Give a bounding box for every leukocyte visible.
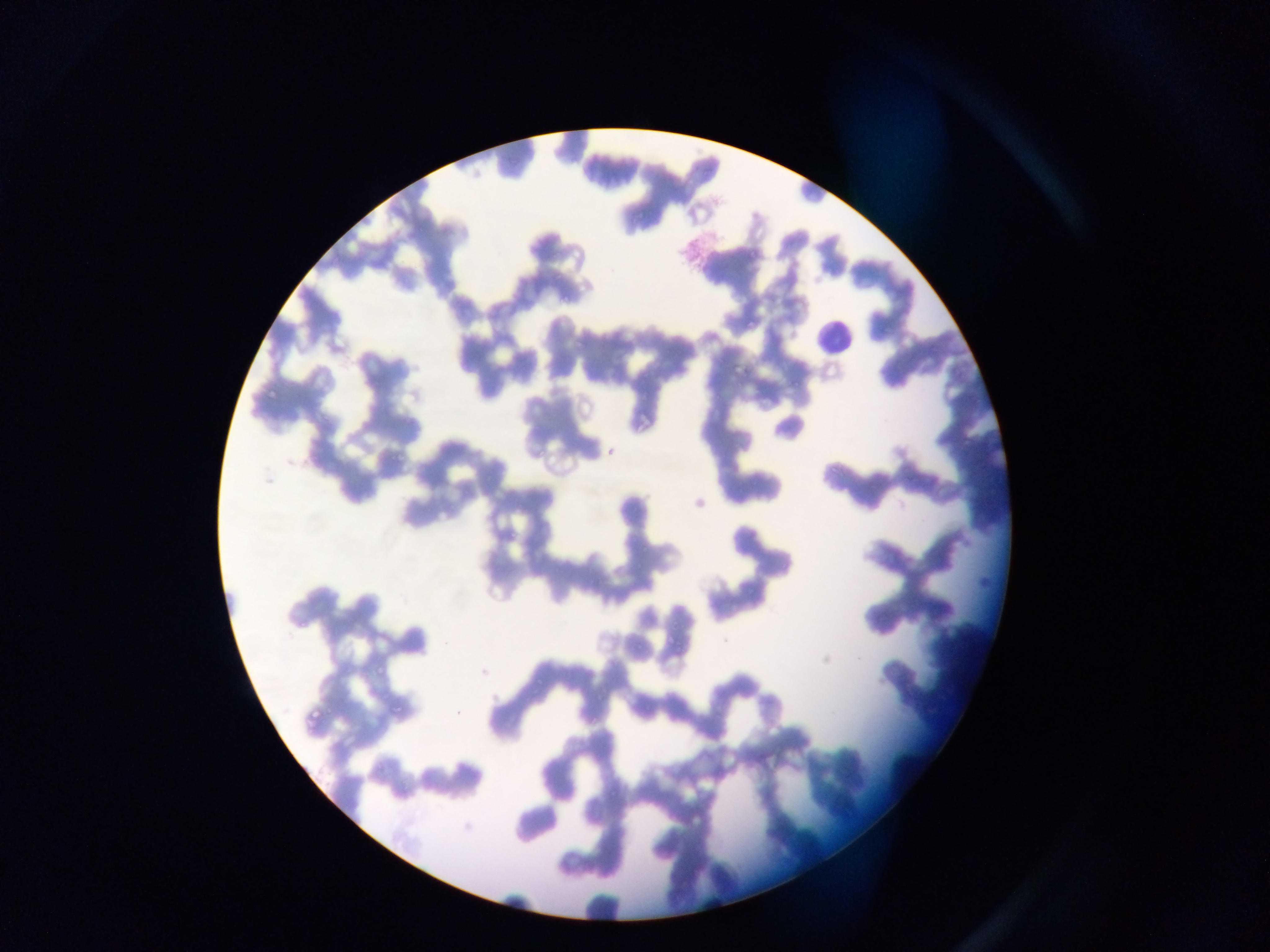
Approximate bounding boxes as [left, top, right, bottom] in pixels.
Leukocytes: [812, 304, 852, 375].

Summary:
  - Plasmodium parasite locations: [568, 245, 579, 262], [743, 253, 762, 263], [775, 291, 791, 312], [744, 318, 758, 329], [882, 331, 891, 336], [729, 358, 745, 376], [262, 389, 279, 402], [601, 442, 620, 456], [386, 448, 413, 467], [667, 625, 676, 649], [477, 659, 494, 684], [372, 663, 387, 677], [531, 668, 555, 699], [387, 700, 399, 720], [301, 705, 317, 732], [396, 784, 410, 800]
  - Capture: mobile-phone photograph through a microscope
  - Image size: 1270×952 pixels
  - Preparation: thin blood smear
  - Country: Ghana
  - Field of view: single